State the blood parasite species.
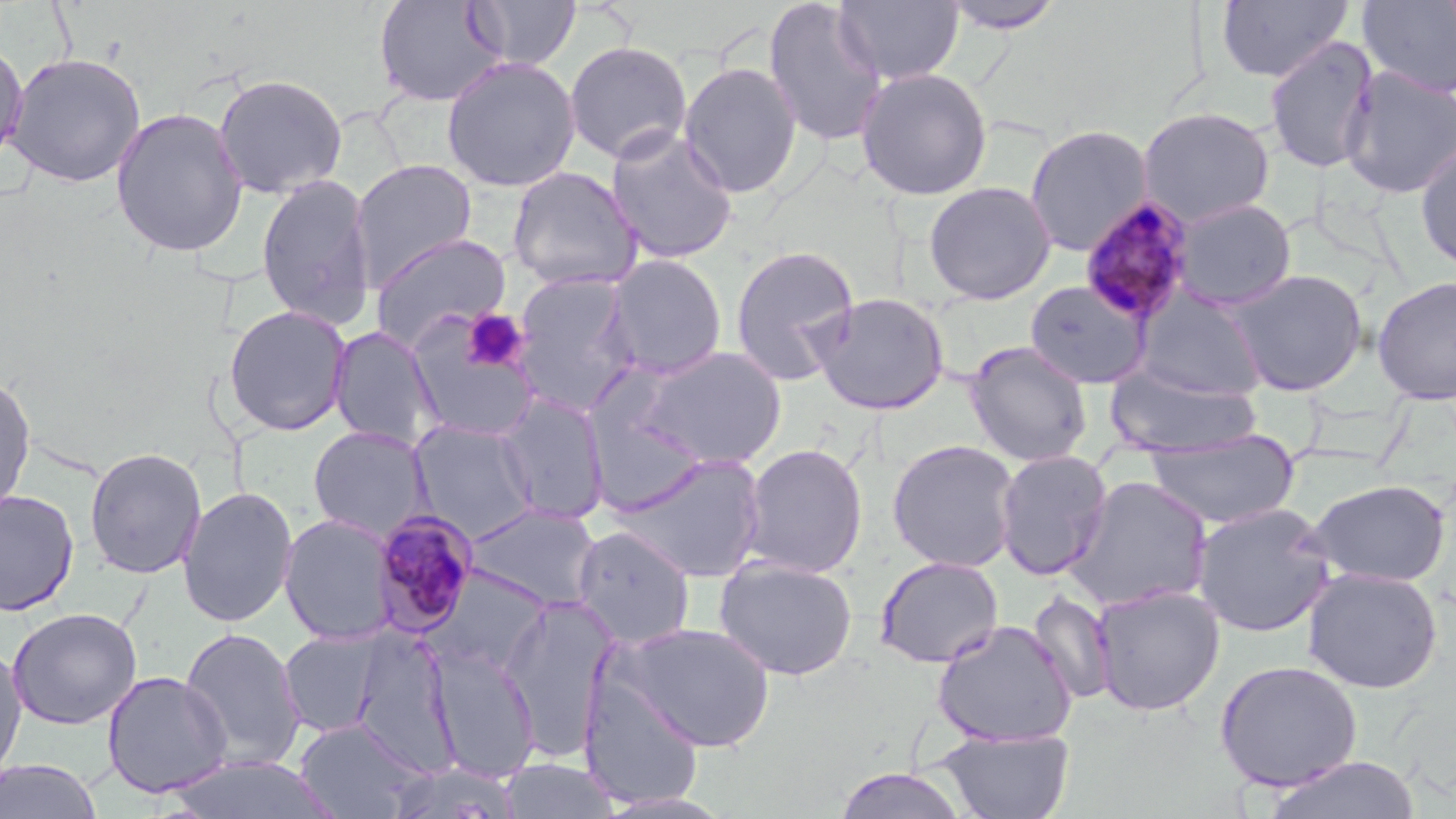

Plasmodium malariae.

field_of_view: one of a larger specimen
platelet_locations: 'approximate bounding boxes as named x1/y1/x2/y2 corners in pixels: (x1=461, y1=309, x2=528, y2=372)'
uninfected_red_blood_cell_locations: 'approximate bounding boxes as named x1/y1/x2/y2 corners in pixels: (x1=372, y1=0, x2=507, y2=108), (x1=762, y1=0, x2=888, y2=147), (x1=834, y1=0, x2=964, y2=86), (x1=1216, y1=0, x2=1353, y2=83), (x1=467, y1=1, x2=581, y2=71), (x1=939, y1=1, x2=1066, y2=34), (x1=1358, y1=1, x2=1456, y2=98), (x1=1264, y1=35, x2=1380, y2=174), (x1=0, y1=38, x2=29, y2=169), (x1=563, y1=40, x2=693, y2=164), (x1=4, y1=52, x2=146, y2=188), (x1=441, y1=56, x2=581, y2=192), (x1=679, y1=61, x2=802, y2=199), (x1=1339, y1=66, x2=1456, y2=200), (x1=855, y1=67, x2=993, y2=200), (x1=212, y1=73, x2=348, y2=199), (x1=110, y1=107, x2=249, y2=258), (x1=1136, y1=107, x2=1276, y2=226), (x1=1024, y1=124, x2=1153, y2=257), (x1=605, y1=127, x2=739, y2=264), (x1=1414, y1=140, x2=1456, y2=274), (x1=348, y1=159, x2=477, y2=289), (x1=507, y1=166, x2=644, y2=291), (x1=255, y1=173, x2=377, y2=330), (x1=922, y1=181, x2=1056, y2=305), (x1=1170, y1=198, x2=1297, y2=311), (x1=369, y1=233, x2=512, y2=352), (x1=729, y1=243, x2=860, y2=386), (x1=603, y1=254, x2=729, y2=380), (x1=1225, y1=268, x2=1369, y2=397), (x1=510, y1=272, x2=640, y2=416), (x1=1372, y1=275, x2=1456, y2=405), (x1=1025, y1=280, x2=1151, y2=389), (x1=1133, y1=287, x2=1267, y2=400), (x1=809, y1=291, x2=951, y2=416), (x1=222, y1=305, x2=353, y2=437), (x1=403, y1=318, x2=542, y2=442), (x1=328, y1=326, x2=444, y2=450), (x1=964, y1=341, x2=1093, y2=467), (x1=636, y1=346, x2=788, y2=469), (x1=1106, y1=366, x2=1262, y2=458), (x1=0, y1=371, x2=36, y2=515), (x1=494, y1=393, x2=611, y2=526), (x1=409, y1=420, x2=538, y2=541), (x1=307, y1=425, x2=433, y2=541), (x1=1144, y1=430, x2=1302, y2=530), (x1=886, y1=439, x2=1021, y2=572), (x1=739, y1=443, x2=868, y2=578), (x1=84, y1=447, x2=207, y2=579), (x1=994, y1=449, x2=1114, y2=581), (x1=610, y1=454, x2=768, y2=583), (x1=1063, y1=475, x2=1214, y2=613), (x1=1307, y1=478, x2=1451, y2=587), (x1=177, y1=485, x2=298, y2=628), (x1=0, y1=488, x2=79, y2=617), (x1=1191, y1=501, x2=1336, y2=638), (x1=464, y1=504, x2=603, y2=612), (x1=279, y1=513, x2=398, y2=646), (x1=571, y1=524, x2=696, y2=648), (x1=712, y1=555, x2=859, y2=681), (x1=873, y1=555, x2=1005, y2=669), (x1=425, y1=567, x2=552, y2=679), (x1=1302, y1=568, x2=1443, y2=693), (x1=1090, y1=583, x2=1225, y2=716), (x1=1027, y1=590, x2=1119, y2=705), (x1=497, y1=594, x2=620, y2=762), (x1=6, y1=607, x2=142, y2=730), (x1=932, y1=619, x2=1078, y2=748), (x1=616, y1=622, x2=776, y2=751), (x1=178, y1=627, x2=305, y2=772), (x1=277, y1=628, x2=388, y2=738), (x1=0, y1=642, x2=28, y2=783), (x1=426, y1=645, x2=542, y2=782), (x1=1214, y1=659, x2=1363, y2=792), (x1=101, y1=670, x2=232, y2=798), (x1=577, y1=671, x2=706, y2=808), (x1=294, y1=718, x2=427, y2=819), (x1=933, y1=728, x2=1076, y2=819), (x1=1260, y1=754, x2=1422, y2=819), (x1=163, y1=755, x2=342, y2=819), (x1=0, y1=758, x2=103, y2=819), (x1=499, y1=758, x2=622, y2=819), (x1=834, y1=767, x2=969, y2=819)'
plasmodium_malariae_infected_red_blood_cell_locations: 'approximate bounding boxes as named x1/y1/x2/y2 corners in pixels: (x1=1080, y1=197, x2=1197, y2=325), (x1=370, y1=508, x2=482, y2=636)'
modality: optical microscopy
preparation: thin blood smear
magnification: 1000x
image_size: 1456×819 pixels
stain: May-Grünwald-Giemsa